Classify this cell by malaria status.
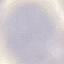

It is uninfected.

image type = automatically extracted cell patch, resized to 64 × 64 pixels
preparation = thin smear
stain = Giemsa
capture = smartphone through the microscope eyepiece